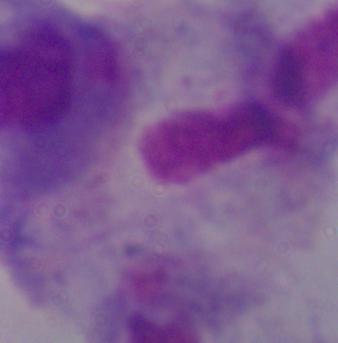
A trichomonad is seen. 1000x magnification. Photomicrograph.